Identify the parasite.
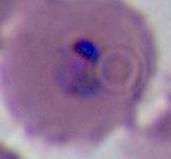

This is Plasmodium.

magnification = 400x or 1000x
modality = micrograph